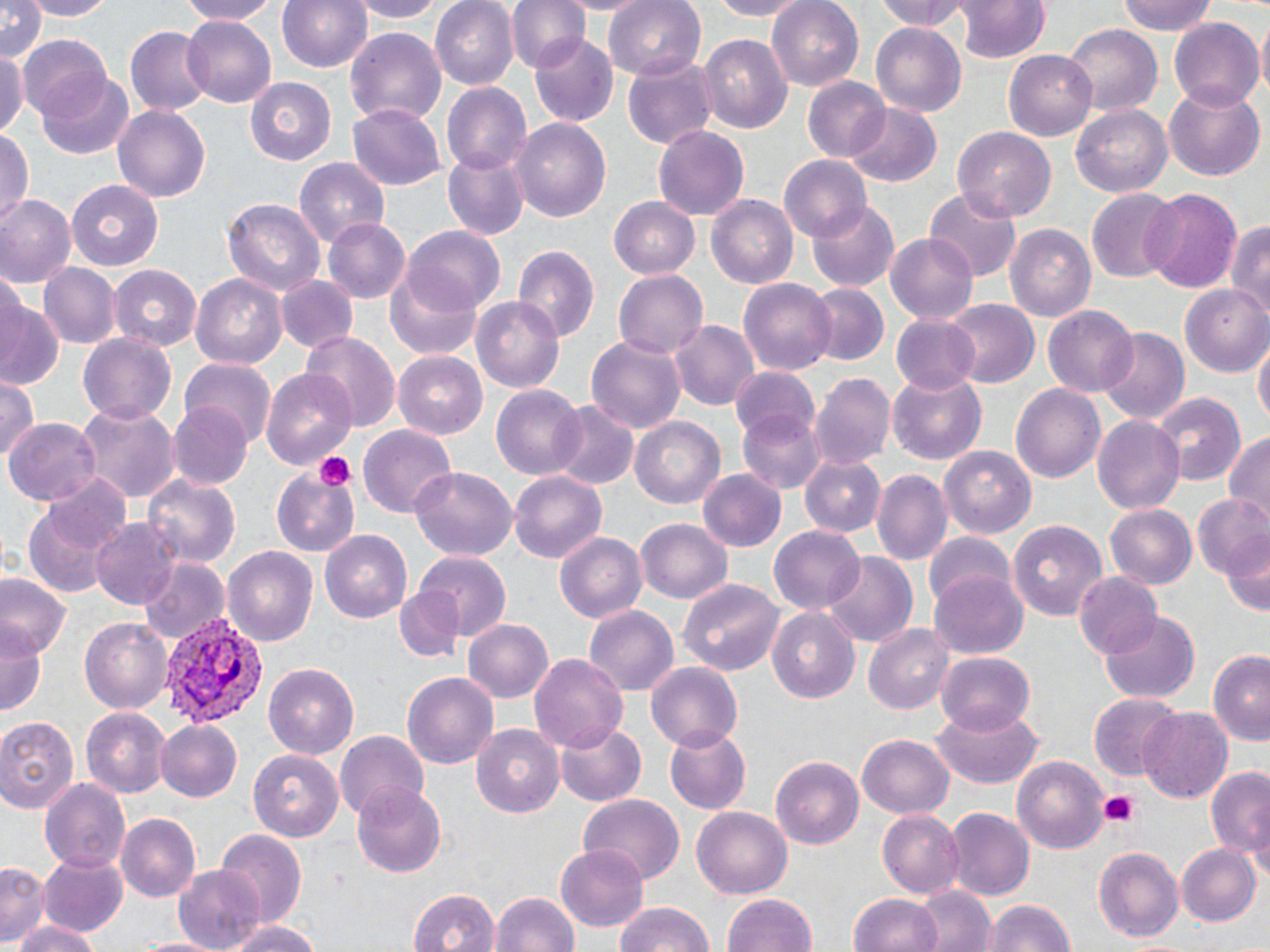

Approximate bounding boxes as [x1, y1, x2, y2] in pixels. Platelet locations: [315, 451, 357, 489], [1100, 793, 1140, 826]. Plasmodium vivax-infected red blood cell locations: [163, 612, 269, 728]. Uninfected red blood cell locations: [0, 0, 46, 64], [23, 0, 118, 20], [173, 0, 287, 24], [278, 0, 372, 74], [349, 0, 444, 22], [430, 0, 517, 89], [507, 0, 590, 73], [606, 0, 706, 79], [699, 0, 811, 20], [767, 0, 865, 91], [870, 0, 974, 34], [1119, 0, 1219, 36], [958, 1, 1050, 65], [182, 15, 276, 108], [1168, 16, 1264, 109], [869, 23, 967, 116], [126, 25, 210, 116], [1064, 25, 1161, 117], [344, 30, 445, 125], [697, 33, 794, 133], [532, 34, 617, 124], [18, 35, 112, 122], [0, 44, 28, 142], [1004, 49, 1098, 139], [622, 59, 715, 150], [39, 71, 136, 158], [245, 75, 336, 165], [803, 77, 890, 163], [442, 83, 532, 175], [1164, 87, 1264, 181], [348, 104, 444, 189], [1070, 104, 1174, 200], [112, 105, 211, 203], [848, 105, 941, 186], [513, 117, 612, 224], [652, 126, 750, 221], [954, 127, 1055, 221], [0, 131, 34, 227], [441, 152, 529, 241], [779, 155, 872, 244], [294, 159, 388, 249], [68, 179, 165, 271], [924, 188, 1022, 281], [1087, 188, 1181, 283], [1138, 188, 1244, 294], [0, 195, 75, 287], [707, 195, 799, 288], [609, 198, 699, 277], [224, 199, 325, 299], [806, 201, 900, 292], [324, 216, 412, 305], [1227, 217, 1270, 320], [1003, 223, 1096, 323], [404, 227, 505, 313], [886, 232, 978, 325], [512, 244, 598, 345], [41, 264, 118, 348], [107, 264, 203, 351], [386, 266, 485, 361], [612, 270, 708, 360], [277, 274, 358, 355], [191, 275, 287, 367], [739, 278, 836, 377], [801, 284, 889, 368], [1182, 286, 1270, 371], [0, 291, 63, 390], [472, 296, 564, 393], [943, 299, 1038, 389], [1041, 304, 1139, 397], [892, 313, 983, 394], [670, 322, 757, 409], [1095, 328, 1192, 424], [301, 329, 400, 432], [75, 331, 177, 426], [587, 336, 686, 435], [1254, 341, 1269, 427], [392, 350, 489, 439], [181, 357, 277, 449], [263, 367, 356, 470], [728, 369, 820, 444], [811, 373, 896, 473], [888, 374, 986, 465], [0, 377, 41, 464], [1010, 382, 1106, 484], [492, 385, 588, 480], [1151, 394, 1244, 488], [169, 403, 253, 491], [74, 405, 181, 503], [549, 405, 639, 491], [740, 409, 826, 495], [629, 416, 726, 509], [1091, 416, 1187, 514], [6, 418, 100, 506], [357, 425, 458, 520], [1223, 430, 1269, 523], [939, 445, 1037, 536], [803, 455, 885, 537], [411, 467, 516, 560], [271, 468, 362, 556], [699, 469, 785, 551], [873, 469, 951, 568], [40, 470, 135, 563], [510, 471, 606, 564], [142, 472, 242, 567], [1190, 494, 1270, 581], [25, 498, 121, 599], [1104, 505, 1197, 590], [637, 517, 732, 603], [1008, 517, 1109, 618], [91, 518, 182, 612], [769, 526, 866, 615], [924, 529, 1014, 613], [320, 530, 411, 623], [555, 530, 646, 624], [1223, 538, 1269, 620], [223, 546, 316, 646], [414, 552, 512, 644], [821, 553, 918, 648], [138, 557, 230, 644], [930, 570, 1029, 660], [0, 572, 68, 657], [1074, 572, 1163, 660], [676, 576, 786, 677], [394, 586, 463, 663], [584, 605, 678, 693], [767, 610, 859, 704], [1098, 612, 1199, 703], [79, 616, 175, 714], [462, 618, 556, 703], [865, 622, 955, 714], [0, 627, 45, 718], [1208, 647, 1270, 744], [937, 651, 1036, 735], [529, 654, 628, 756], [646, 660, 742, 751], [264, 662, 357, 758], [403, 673, 498, 771], [1088, 694, 1183, 782], [932, 706, 1046, 792], [80, 707, 173, 798], [1138, 708, 1232, 805], [0, 714, 82, 812], [155, 718, 243, 802], [553, 720, 647, 807], [471, 724, 563, 819], [661, 724, 750, 814], [334, 730, 431, 818], [857, 736, 954, 817], [250, 749, 343, 842], [1012, 755, 1110, 856], [771, 756, 863, 849], [1205, 767, 1269, 865], [40, 778, 132, 874], [353, 786, 448, 877], [580, 794, 684, 882], [691, 805, 792, 899], [946, 808, 1034, 902], [878, 809, 964, 897], [117, 814, 200, 901], [215, 831, 306, 930], [1176, 841, 1261, 926], [555, 843, 649, 932], [1092, 845, 1184, 942], [39, 854, 130, 938], [0, 860, 48, 945], [173, 865, 263, 950], [915, 884, 995, 952], [406, 888, 501, 952], [489, 891, 580, 952], [850, 892, 944, 952], [723, 893, 818, 952], [981, 899, 1074, 952], [611, 901, 719, 952], [12, 919, 102, 952], [222, 921, 328, 952]. Slide-level diagnosis: Plasmodium vivax. Light microscopy. Thin blood film. May-Grünwald-Giemsa stain. Image is 1270×952 pixels. 1000x magnification. One field of a larger specimen.